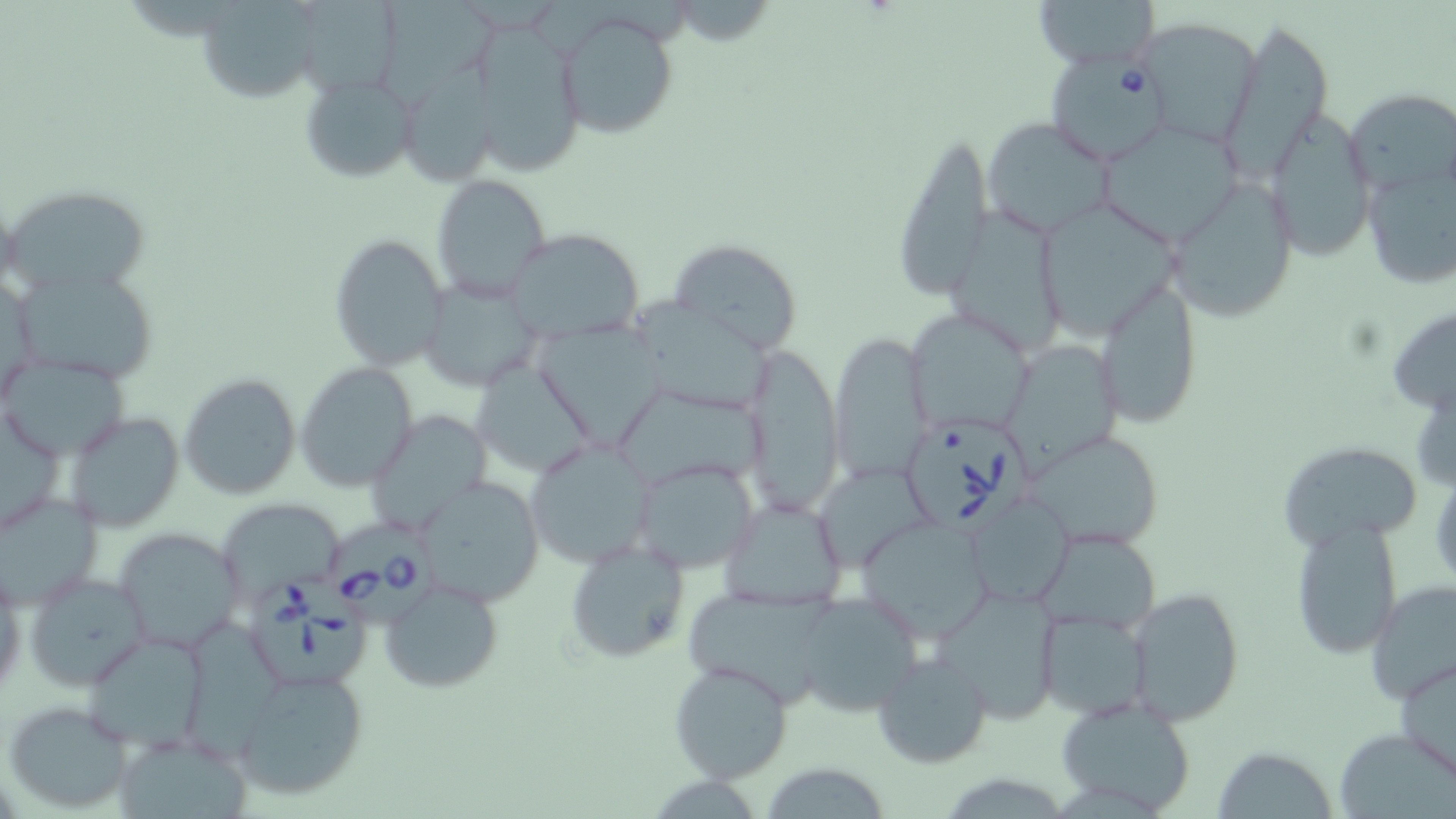

Summary:
  - Coordinate format: approximate bounding boxes as (x1,y1)-(x2,y2) corner pairs in pixels
  - Babesia divergens-infected red blood cell locations: (1044,50)-(1175,166), (903,420)-(1034,529), (322,518)-(442,621), (251,576)-(374,692)
  - Uninfected red blood cell locations: (195,0)-(327,103), (301,0)-(402,103), (1031,0)-(1160,72), (376,1)-(501,108), (552,8)-(681,141), (1219,15)-(1334,180), (1135,17)-(1264,144), (477,24)-(586,181), (401,53)-(510,192), (297,72)-(419,185), (1346,89)-(1455,200), (1263,109)-(1376,262), (980,117)-(1117,239), (1097,119)-(1246,245), (887,127)-(995,303), (1357,156)-(1456,292), (1163,172)-(1301,323), (432,174)-(553,301), (5,184)-(152,298), (1035,197)-(1185,343), (944,205)-(1066,356), (504,228)-(645,342), (329,233)-(450,371), (667,238)-(805,355), (15,264)-(161,384), (1095,278)-(1203,424), (418,279)-(545,391), (633,291)-(772,413), (1385,302)-(1456,418), (907,309)-(1036,436), (534,321)-(671,452), (829,331)-(932,485), (1003,337)-(1124,469), (741,342)-(845,517), (2,356)-(128,461), (468,358)-(595,479), (296,362)-(417,491), (1413,369)-(1456,498), (179,373)-(303,501), (612,389)-(769,496), (1,406)-(67,537), (63,410)-(184,533), (364,410)-(491,535), (1020,428)-(1170,553), (524,438)-(658,569), (1277,442)-(1426,556), (629,456)-(760,575), (816,467)-(938,564), (1430,468)-(1456,596), (417,476)-(546,606), (0,489)-(104,607), (966,491)-(1075,608), (720,497)-(848,611), (216,499)-(343,600), (861,517)-(991,639), (1288,518)-(1405,661), (113,526)-(245,654), (1035,527)-(1161,634), (564,537)-(692,664), (24,570)-(152,692), (379,575)-(505,695), (1366,580)-(1456,703), (936,585)-(1062,722), (1124,587)-(1249,727), (685,590)-(824,711), (791,592)-(926,719), (1038,607)-(1155,719), (184,621)-(291,758), (82,631)-(210,752), (870,651)-(993,768), (1395,654)-(1456,781), (668,659)-(793,784), (234,667)-(372,802), (1054,695)-(1197,817), (4,699)-(137,814), (1335,728)-(1454,818), (116,730)-(252,819), (1211,746)-(1340,819), (754,761)-(897,818)
  - Slide-level diagnosis: Babesia divergens
  - Modality: light microscopy
  - Field of view: one of a larger specimen
  - Preparation: thin blood film
  - Stain: May-Grünwald-Giemsa
  - Magnification: 1000x
  - Image size: 1456×819 pixels